Name the parasite shown.
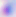
This is Toxoplasma gondii.

Photomicrograph. Captured at 400x magnification.